Locate every blood parasite and identify its species.
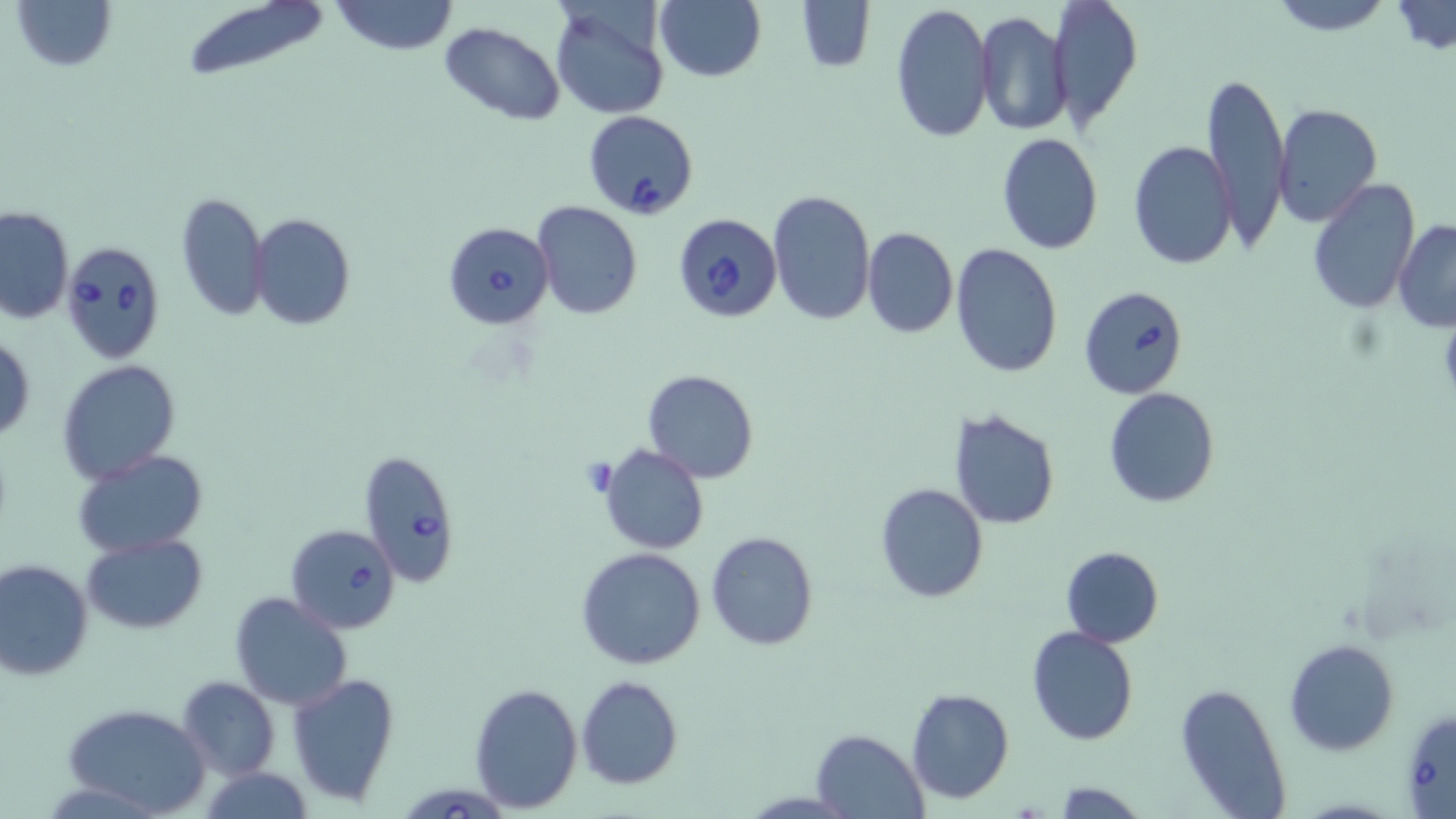
Approximate bounding boxes as (x1, y1, x2, y2) in pixels.
Babesia divergens-infected red blood cells: (583, 109, 699, 219), (672, 213, 783, 323), (442, 220, 554, 329), (61, 240, 166, 363), (1078, 285, 1189, 401), (358, 449, 460, 586), (286, 524, 401, 634), (404, 786, 505, 819).
No Plasmodium falciparum, Plasmodium ovale, Plasmodium malariae, Plasmodium vivax, or Trypanosoma brucei observed.

Uninfected red blood cell locations: (9, 0, 119, 73), (330, 0, 459, 56), (1048, 0, 1143, 132), (1269, 0, 1394, 36), (179, 1, 333, 83), (652, 1, 767, 83), (794, 1, 877, 74), (888, 1, 994, 142), (548, 2, 670, 121), (1389, 2, 1454, 55), (975, 10, 1073, 136), (440, 21, 566, 124), (1201, 70, 1291, 252), (1273, 104, 1383, 228), (996, 133, 1104, 256), (1128, 139, 1238, 271), (1307, 178, 1421, 314), (768, 189, 878, 327), (176, 191, 268, 322), (535, 202, 642, 319), (1, 207, 73, 324), (249, 213, 355, 331), (1393, 219, 1456, 330), (861, 227, 959, 339), (951, 242, 1063, 378), (1, 332, 36, 444), (56, 359, 181, 484), (642, 369, 759, 483), (1103, 387, 1220, 509), (948, 407, 1062, 531), (595, 443, 710, 556), (72, 450, 209, 558), (874, 482, 990, 603), (705, 530, 820, 651), (82, 534, 207, 634), (1060, 546, 1164, 647), (576, 547, 706, 670), (0, 558, 94, 681), (229, 592, 354, 711), (1026, 626, 1140, 747), (1285, 638, 1398, 755), (287, 672, 401, 806), (576, 675, 683, 789), (176, 676, 279, 781), (467, 681, 583, 814), (1173, 681, 1292, 817), (905, 687, 1014, 804), (61, 702, 211, 818), (1400, 706, 1455, 818), (810, 729, 928, 818), (199, 765, 315, 819), (1053, 781, 1144, 817). Platelet locations: (581, 456, 620, 498). Slide-level diagnosis: Babesia divergens. May-Grünwald-Giemsa-stained preparation. Image is 1456×819 pixels. Thin blood film. 1000x magnification. One field of a larger specimen. Optical microscopy.